Give the extent of all uninfected red blood cells.
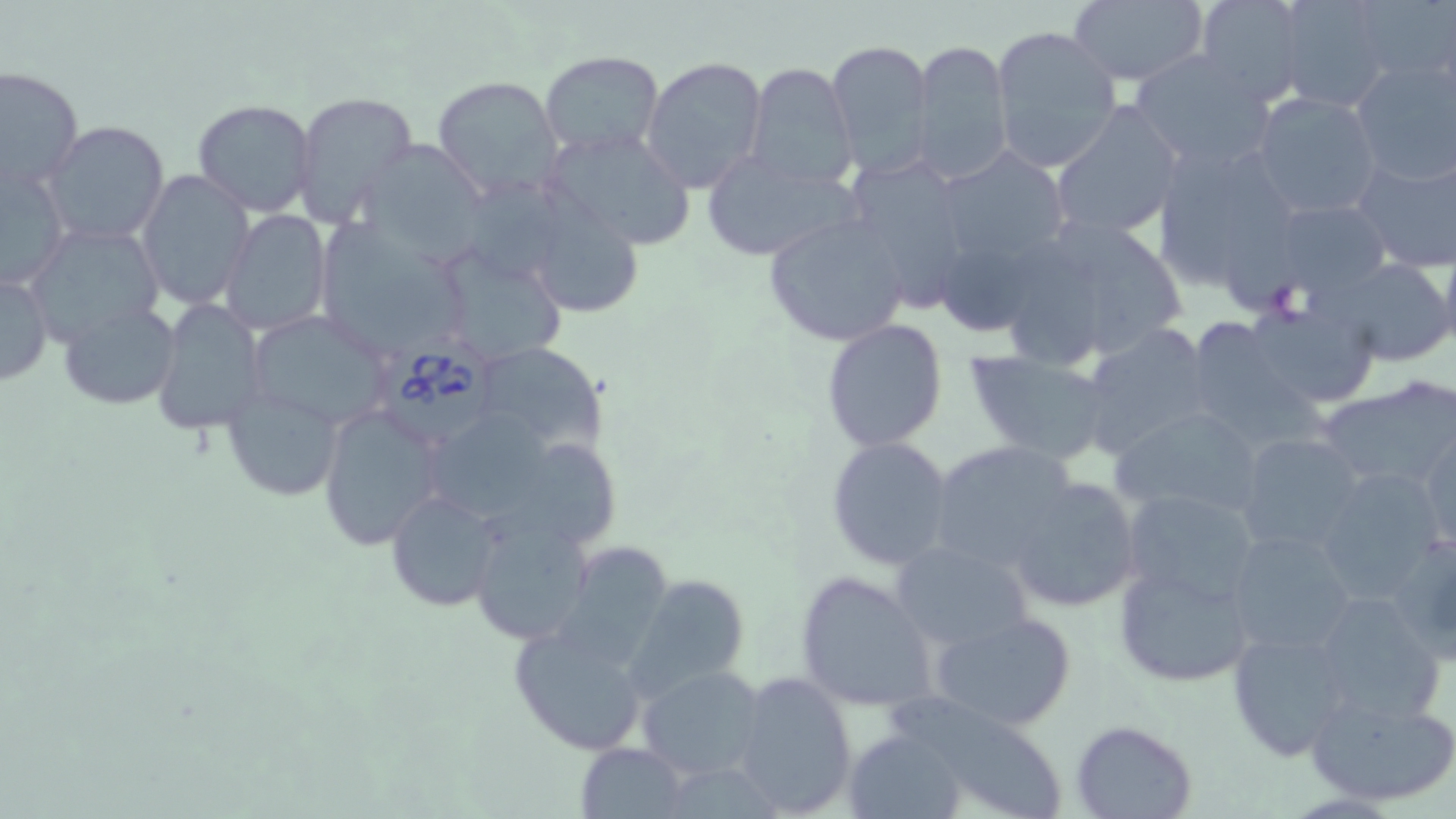

Approximate bounding boxes as [x1, y1, x2, y2] in pixels.
Uninfected red blood cells: [1069, 0, 1209, 86], [1192, 0, 1309, 105], [1276, 0, 1393, 109], [1353, 1, 1455, 89], [991, 24, 1123, 173], [911, 38, 1012, 183], [826, 39, 935, 176], [540, 51, 664, 157], [1129, 51, 1277, 172], [642, 55, 768, 192], [1349, 56, 1456, 186], [744, 63, 858, 190], [0, 66, 83, 194], [431, 74, 563, 202], [291, 90, 418, 225], [1249, 91, 1383, 219], [192, 99, 318, 218], [1050, 103, 1184, 242], [41, 121, 169, 248], [539, 125, 696, 252], [1151, 136, 1311, 303], [355, 139, 489, 261], [932, 147, 1075, 272], [1352, 148, 1456, 272], [701, 151, 857, 264], [840, 154, 976, 308], [0, 160, 70, 290], [136, 168, 255, 309], [469, 176, 576, 280], [527, 196, 643, 319], [1265, 197, 1395, 299], [220, 209, 333, 337], [763, 213, 912, 348], [1063, 222, 1185, 351], [25, 224, 165, 345], [316, 224, 469, 360], [1438, 241, 1456, 362], [431, 244, 568, 367], [1010, 252, 1104, 362], [949, 256, 1035, 333], [1325, 257, 1454, 366], [1, 269, 52, 387], [1243, 296, 1382, 413], [151, 298, 266, 435], [58, 301, 181, 408], [1193, 308, 1324, 441], [246, 309, 391, 432], [820, 320, 949, 452], [1080, 324, 1215, 457], [473, 342, 606, 457], [964, 350, 1112, 466], [1314, 379, 1455, 497], [221, 381, 345, 503], [319, 401, 450, 549], [1110, 406, 1266, 521], [431, 411, 563, 526], [1418, 423, 1455, 554], [1234, 433, 1364, 555], [825, 436, 955, 571], [926, 440, 1081, 577], [521, 446, 625, 548], [1311, 467, 1448, 602], [1007, 476, 1142, 611], [1119, 488, 1261, 608], [386, 489, 504, 611], [468, 515, 595, 645], [1225, 530, 1357, 659], [890, 539, 1032, 655], [553, 542, 676, 671], [1115, 560, 1256, 689], [794, 570, 937, 713], [627, 575, 751, 700], [1307, 592, 1446, 722], [929, 608, 1078, 733], [509, 622, 652, 756], [1225, 629, 1354, 761], [637, 665, 768, 780], [730, 671, 857, 817], [1305, 688, 1456, 808], [897, 692, 1062, 819], [1069, 720, 1199, 819], [844, 730, 965, 818], [577, 741, 688, 816].

slide-level diagnosis = Babesia divergens
modality = light microscopy
magnification = 1000x
field of view = single
Babesia divergens-infected red blood cell locations = approximate bounding boxes as [x1, y1, x2, y2] in pixels: [381, 335, 497, 453]
preparation = thin blood film
image size = 1456×819 pixels
stain = May-Grünwald-Giemsa